Locate and identify every blood parasite.
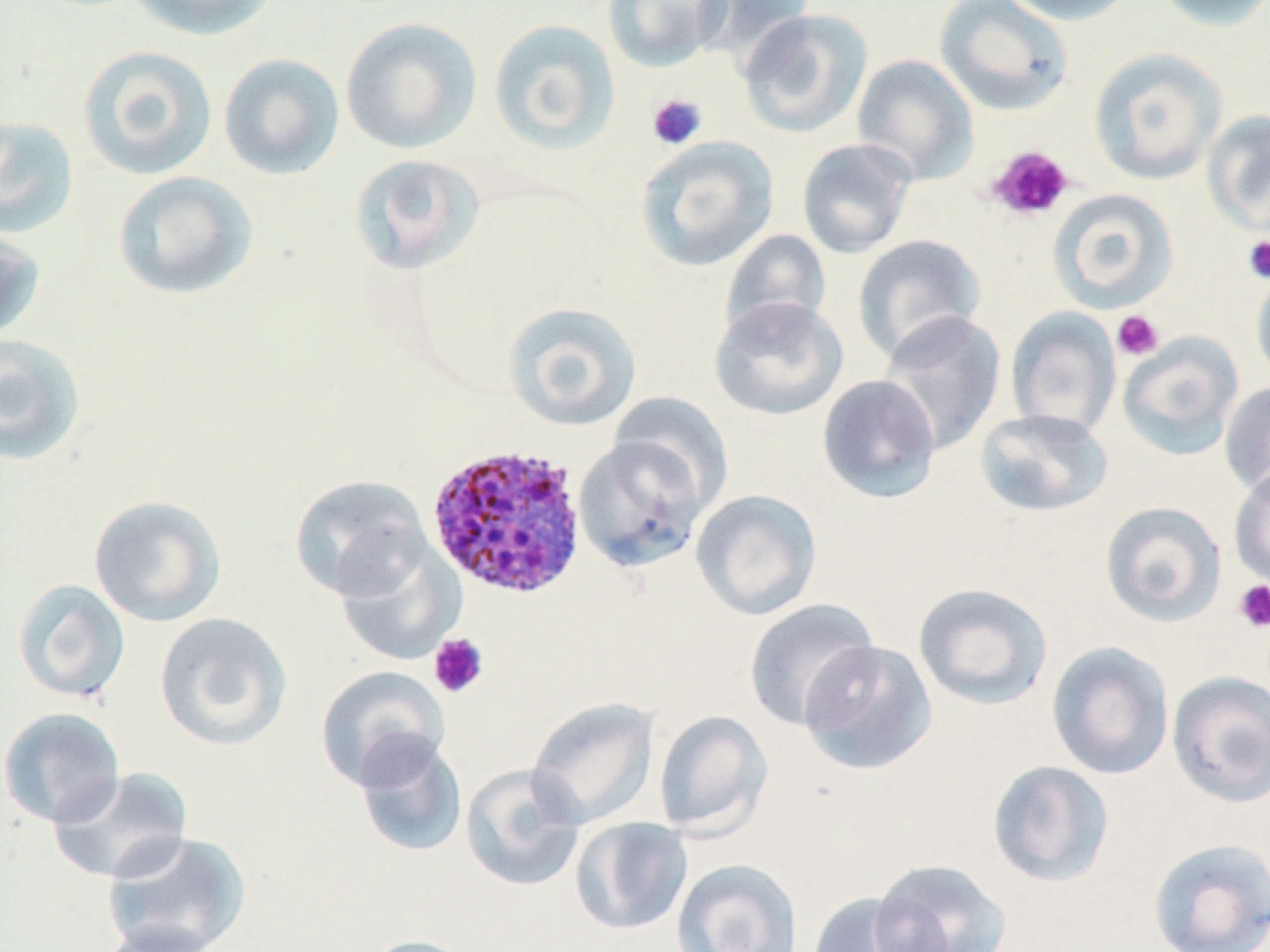
Approximate bounding boxes as (x1, y1, x2, y2) in pixels.
Plasmodium ovale-infected red blood cells: (424, 442, 588, 599).
No Plasmodium falciparum, Plasmodium malariae, Plasmodium vivax, Babesia divergens, or Trypanosoma brucei observed.

Uninfected red blood cell locations: (123, 0, 278, 40), (602, 0, 731, 73), (690, 0, 817, 63), (934, 0, 1074, 116), (995, 0, 1138, 26), (1148, 0, 1270, 33), (737, 8, 872, 138), (340, 17, 482, 154), (488, 18, 621, 154), (77, 45, 218, 181), (1088, 47, 1227, 185), (218, 53, 345, 180), (851, 54, 978, 185), (1203, 110, 1270, 236), (0, 115, 79, 239), (634, 135, 779, 271), (796, 137, 917, 259), (349, 153, 485, 275), (112, 170, 258, 300), (1047, 188, 1179, 313), (0, 229, 46, 341), (719, 229, 832, 342), (852, 234, 987, 364), (1251, 264, 1270, 387), (709, 295, 849, 421), (502, 301, 642, 432), (1006, 308, 1121, 439), (877, 310, 1006, 455), (1117, 331, 1245, 461), (0, 333, 87, 466), (816, 374, 942, 504), (1219, 381, 1270, 500), (609, 392, 734, 511), (974, 408, 1114, 517), (573, 431, 712, 573), (1229, 466, 1270, 589), (289, 473, 431, 602), (691, 489, 822, 621), (88, 494, 227, 627), (1100, 501, 1226, 627), (335, 540, 466, 666), (12, 579, 131, 703), (913, 582, 1054, 711), (743, 598, 880, 731), (154, 612, 293, 751), (799, 639, 938, 776), (1047, 641, 1174, 780), (315, 665, 450, 790), (1167, 670, 1270, 808), (526, 696, 660, 829), (0, 707, 126, 827), (653, 709, 773, 839), (352, 733, 468, 858), (986, 759, 1115, 888), (459, 764, 585, 892), (47, 766, 195, 884), (570, 817, 693, 936), (101, 830, 253, 952), (1148, 837, 1270, 952), (672, 858, 801, 952), (869, 858, 1012, 952), (806, 892, 941, 952), (95, 922, 224, 952), (361, 934, 479, 952). Platelet locations: (646, 93, 708, 151), (986, 145, 1074, 222), (1242, 235, 1270, 284), (1111, 310, 1164, 361), (1233, 578, 1270, 633), (428, 632, 489, 699). Slide-level diagnosis: Plasmodium ovale. Optical microscopy. Single field of view. 1000x magnification. May-Grünwald-Giemsa-stained preparation. Thin blood film. Image is 1270×952 pixels.